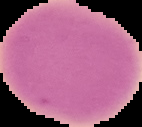

image type = segmented cell region with the area outside set to black
preparation = thin blood smear
image size = 142×127 pixels
result = no malaria parasites seen